Report the malaria status of this cell.
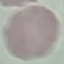

Uninfected.

Summary:
  - Stain: Giemsa
  - Image type: automatically extracted cell patch, resized to 64 × 64 pixels
  - Preparation: thin blood smear
  - Capture: smartphone through the microscope eyepiece